Comment on the morphology of the red blood cells.
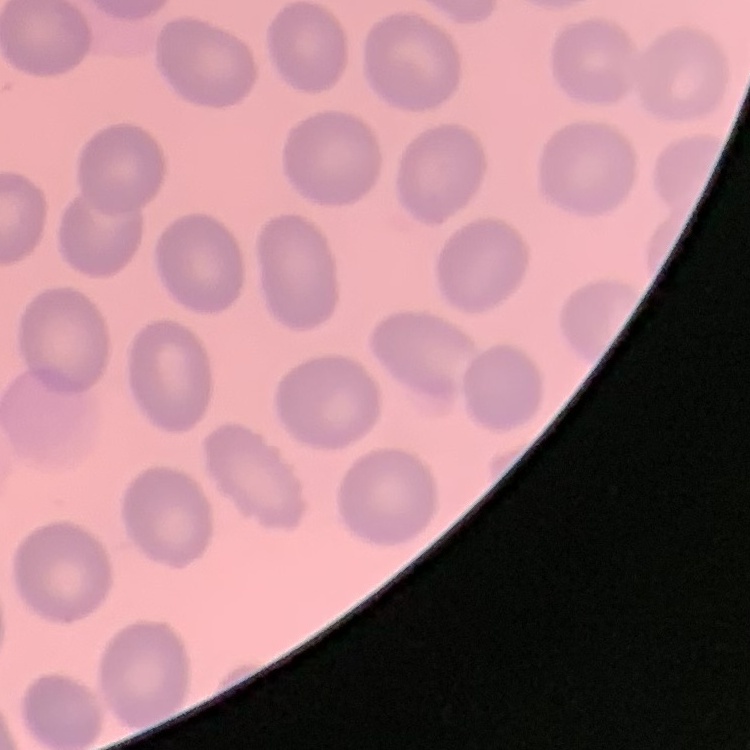
No rouleaux formation.

image type = square crop of a larger photomicrograph
preparation = thin blood film
stain = Field's or Giemsa